Identify the parasite.
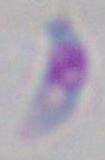
This is Toxoplasma gondii.

{
  "magnification": "1000x",
  "modality": "micrograph"
}